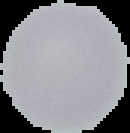
Summary:
  - Image type: segmented cell region with the area outside set to black
  - Image size: 130×133 pixels
  - Result: no Plasmodium parasites seen
  - Preparation: thin blood film